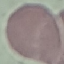

Summary:
  - Result: no malaria parasites seen
  - Preparation: thin blood smear
  - Capture: smartphone through the microscope eyepiece
  - Image type: automatically extracted cell patch, resized to 64 × 64 pixels
  - Stain: Giemsa